Report the malaria status of this cell.
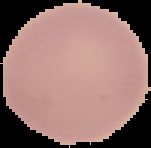

Uninfected.

Image is 151×148 pixels. From a thin blood film. Segmented cell region on a black background.